Classify this cell by malaria status.
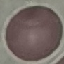
Uninfected.

Giemsa stain. Cell patch, automatically extracted from a larger field of view and resized to 64 × 64 pixels. Acquired by smartphone through the microscope eyepiece. Thin smear of blood.